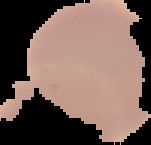

Segmented cell region on a black background. Image is 151×145 pixels. Result: no malaria parasites detected. From a thin blood smear.